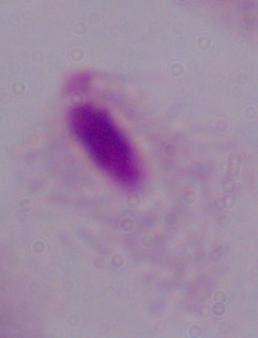 Photomicrograph. A trichomonad is seen. Captured at 1000x magnification.